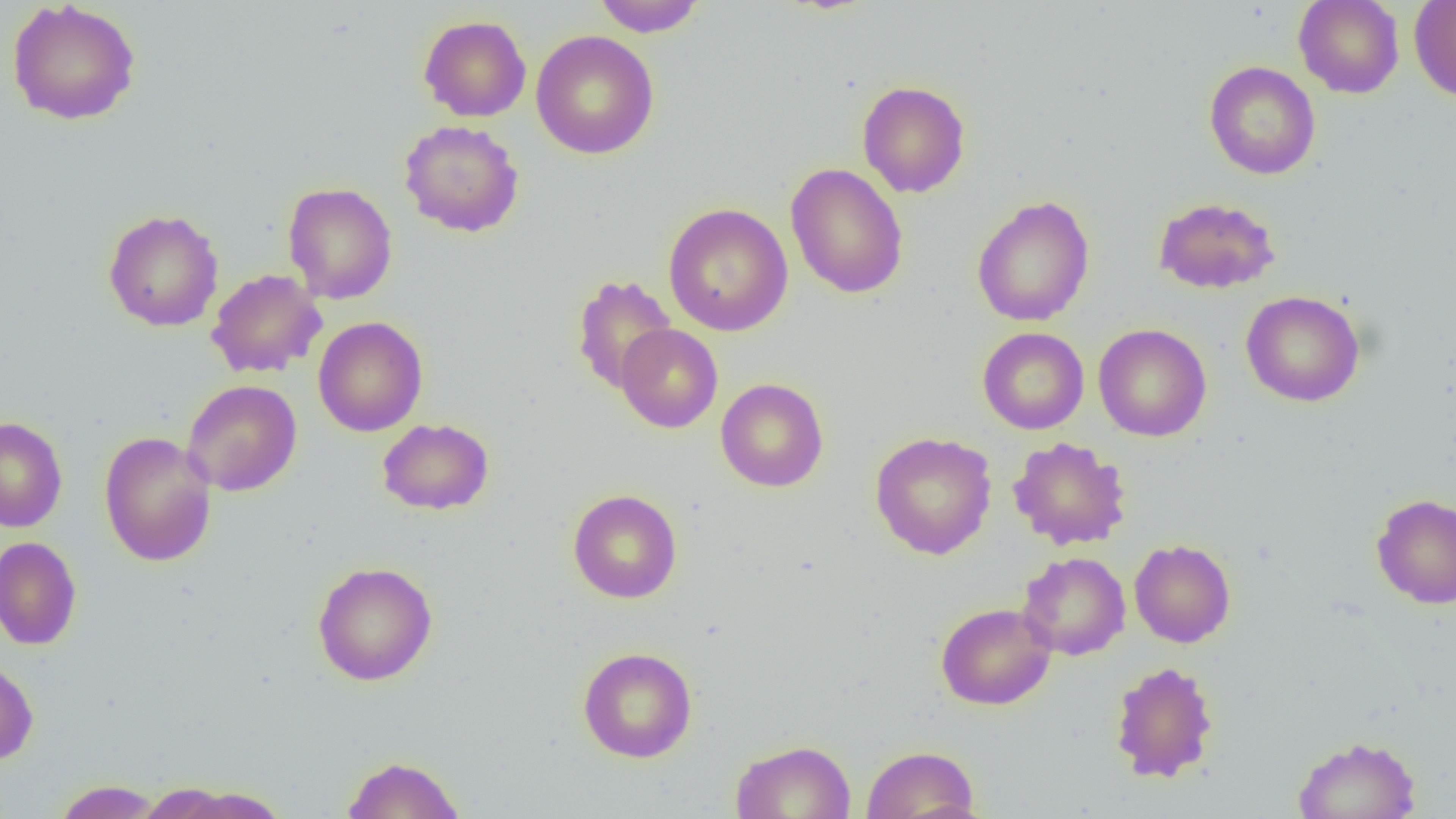

slide-level diagnosis = negative for blood parasites
uninfected red blood cell locations = approximate bounding boxes as named x1/y1/x2/y2 corners in pixels: (x1=592, y1=0, x2=707, y2=37), (x1=1293, y1=0, x2=1405, y2=98), (x1=1409, y1=0, x2=1456, y2=103), (x1=6, y1=1, x2=142, y2=126), (x1=418, y1=15, x2=531, y2=122), (x1=531, y1=30, x2=659, y2=159), (x1=1204, y1=60, x2=1320, y2=179), (x1=857, y1=80, x2=970, y2=198), (x1=399, y1=120, x2=524, y2=237), (x1=785, y1=163, x2=908, y2=299), (x1=282, y1=182, x2=398, y2=304), (x1=971, y1=195, x2=1095, y2=327), (x1=1153, y1=197, x2=1280, y2=295), (x1=663, y1=202, x2=793, y2=336), (x1=103, y1=208, x2=223, y2=332), (x1=206, y1=269, x2=327, y2=378), (x1=570, y1=274, x2=678, y2=395), (x1=1241, y1=290, x2=1365, y2=407), (x1=313, y1=316, x2=428, y2=437), (x1=1094, y1=323, x2=1212, y2=442), (x1=616, y1=324, x2=723, y2=433), (x1=977, y1=327, x2=1089, y2=435), (x1=715, y1=378, x2=829, y2=492), (x1=182, y1=379, x2=302, y2=496), (x1=0, y1=417, x2=68, y2=532), (x1=377, y1=418, x2=494, y2=515), (x1=98, y1=431, x2=216, y2=568), (x1=869, y1=431, x2=997, y2=560), (x1=1007, y1=437, x2=1132, y2=550), (x1=567, y1=488, x2=683, y2=604), (x1=1371, y1=493, x2=1456, y2=609), (x1=0, y1=537, x2=82, y2=650), (x1=1128, y1=538, x2=1236, y2=647), (x1=1017, y1=551, x2=1131, y2=660), (x1=312, y1=561, x2=438, y2=686), (x1=935, y1=602, x2=1056, y2=710), (x1=577, y1=646, x2=697, y2=763), (x1=0, y1=656, x2=38, y2=765), (x1=1109, y1=660, x2=1220, y2=784), (x1=1293, y1=735, x2=1421, y2=819), (x1=730, y1=739, x2=856, y2=819), (x1=861, y1=745, x2=979, y2=819), (x1=341, y1=754, x2=466, y2=818), (x1=53, y1=780, x2=164, y2=818), (x1=162, y1=785, x2=293, y2=819)
preparation = thin blood film
modality = optical microscopy
image size = 1456×819 pixels
magnification = 1000x
field of view = single